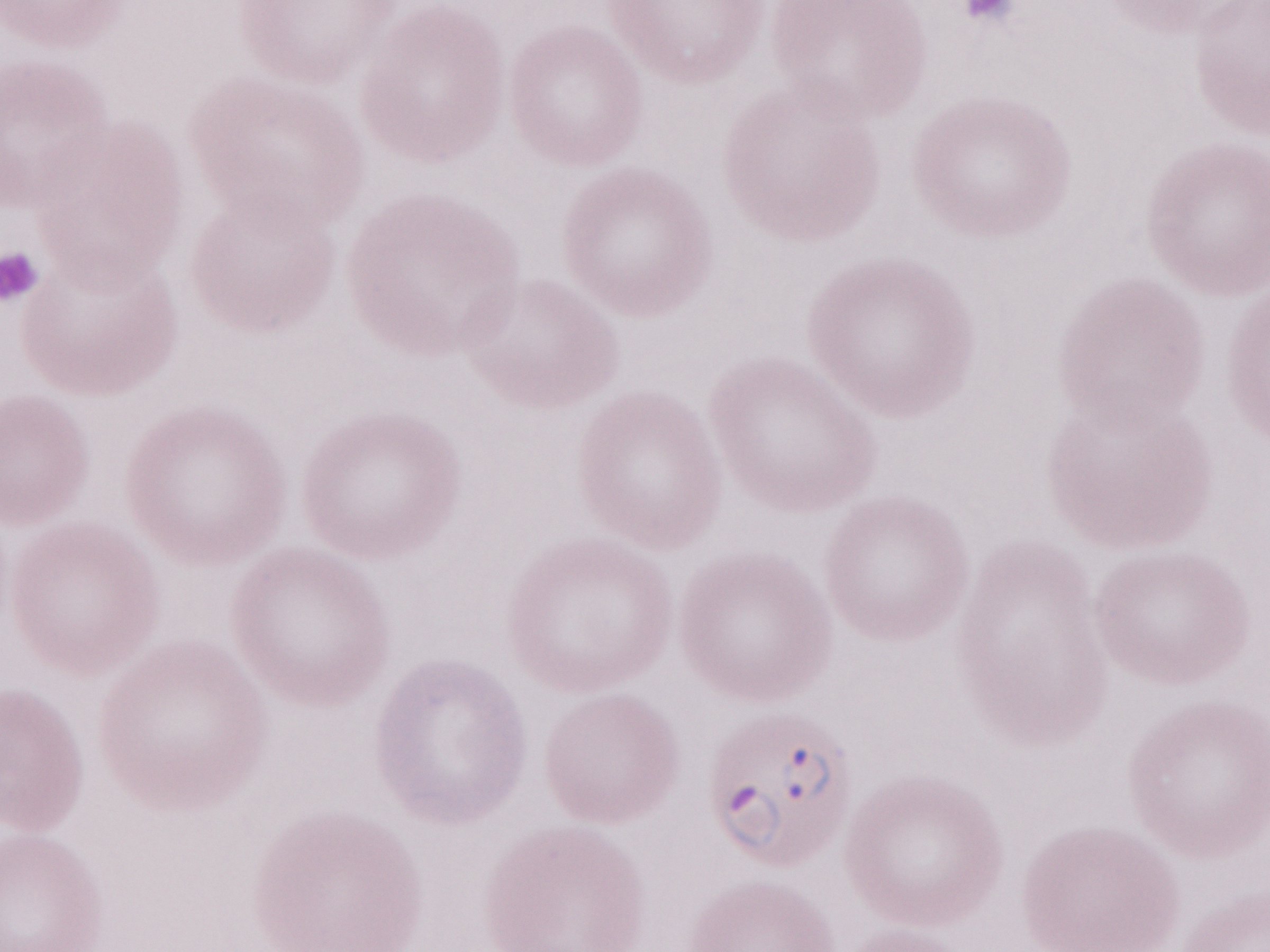

Olympus BX43 microscope and DP73 digital camera. May-Grünwald-Giemsa (MGG) stain. One field of this slide. Patient-level malaria diagnosis: positive. Thin blood film. Magnification: 1,000x. Image is 1270×952 pixels.